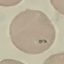

malaria status = parasitized
capture = smartphone through the microscope eyepiece
image type = cell patch, automatically extracted from a larger field of view and resized to 64 × 64 pixels
stain = Giemsa
preparation = thin smear